Comment on the morphology of the red blood cells.
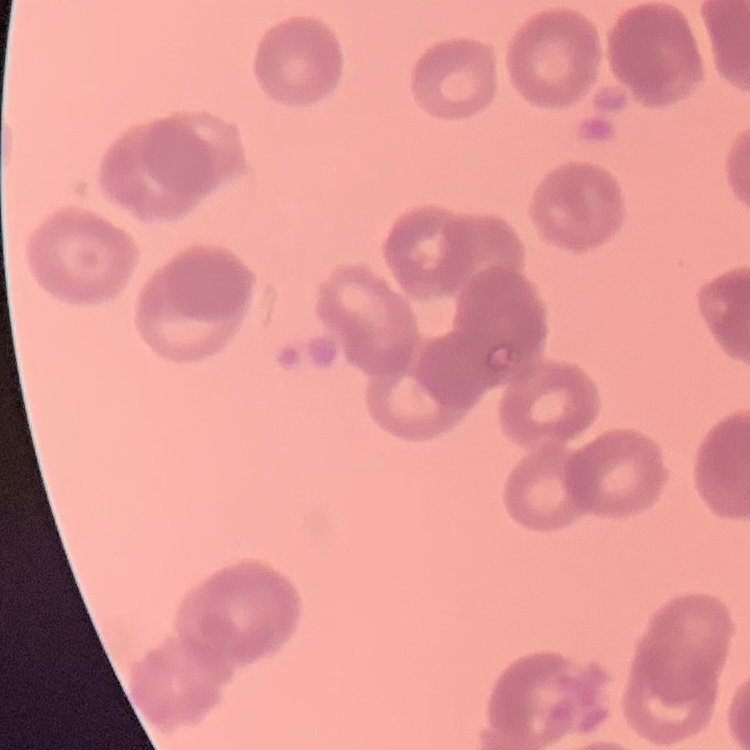
They show rouleaux formation.

Thin peripheral smear. Field's or Giemsa stain. Square crop of a larger photomicrograph.